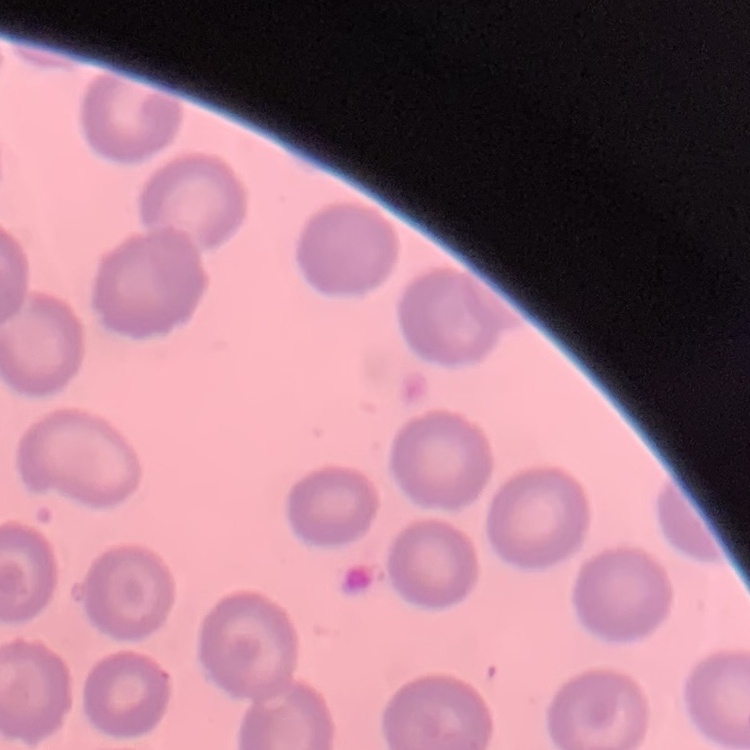

erythrocyte morphology = no rouleaux formation
preparation = thin peripheral smear
stain = Field's or Giemsa
image type = one tile cut from a larger photomicrograph